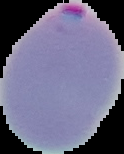
Cell region segmented out of the field of view; the surrounding area is masked to black. Image is 124×154 pixels. Malaria status: parasitized. From a thin blood film.